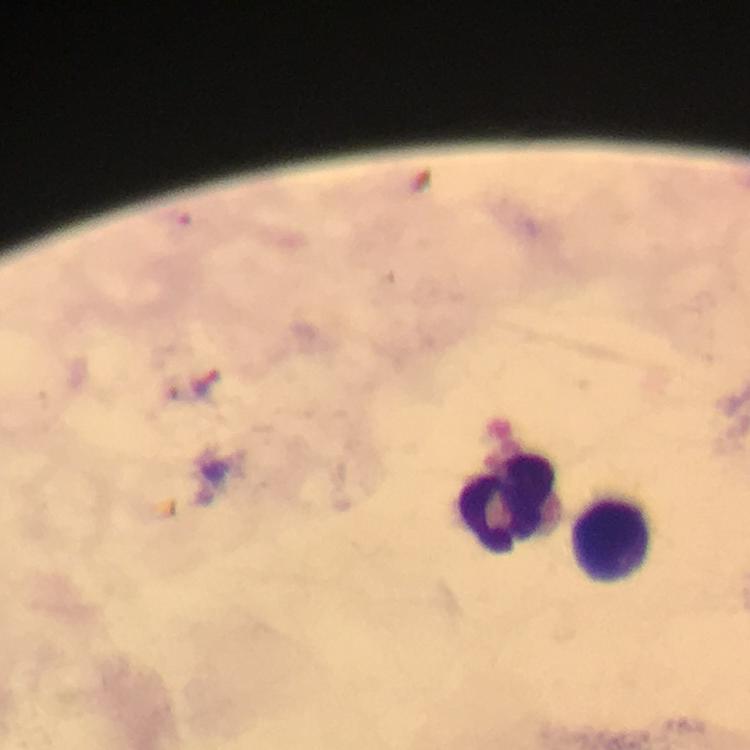

Approximate centers as (x, y) in pixels.
Summary:
  - Leukocyte locations: (508, 507), (609, 541)
  - Magnification: 100x
  - Preparation: thick blood smear
  - Context: from a malaria diagnostic workup
  - Cropped from: a single field of view
  - Capture: smartphone photograph through a microscope
  - Malaria parasites: none detected
  - Stain: Giemsa
  - Immersion oil: applied
  - Image size: 750×750 pixels